Locate every blood parasite and identify its species.
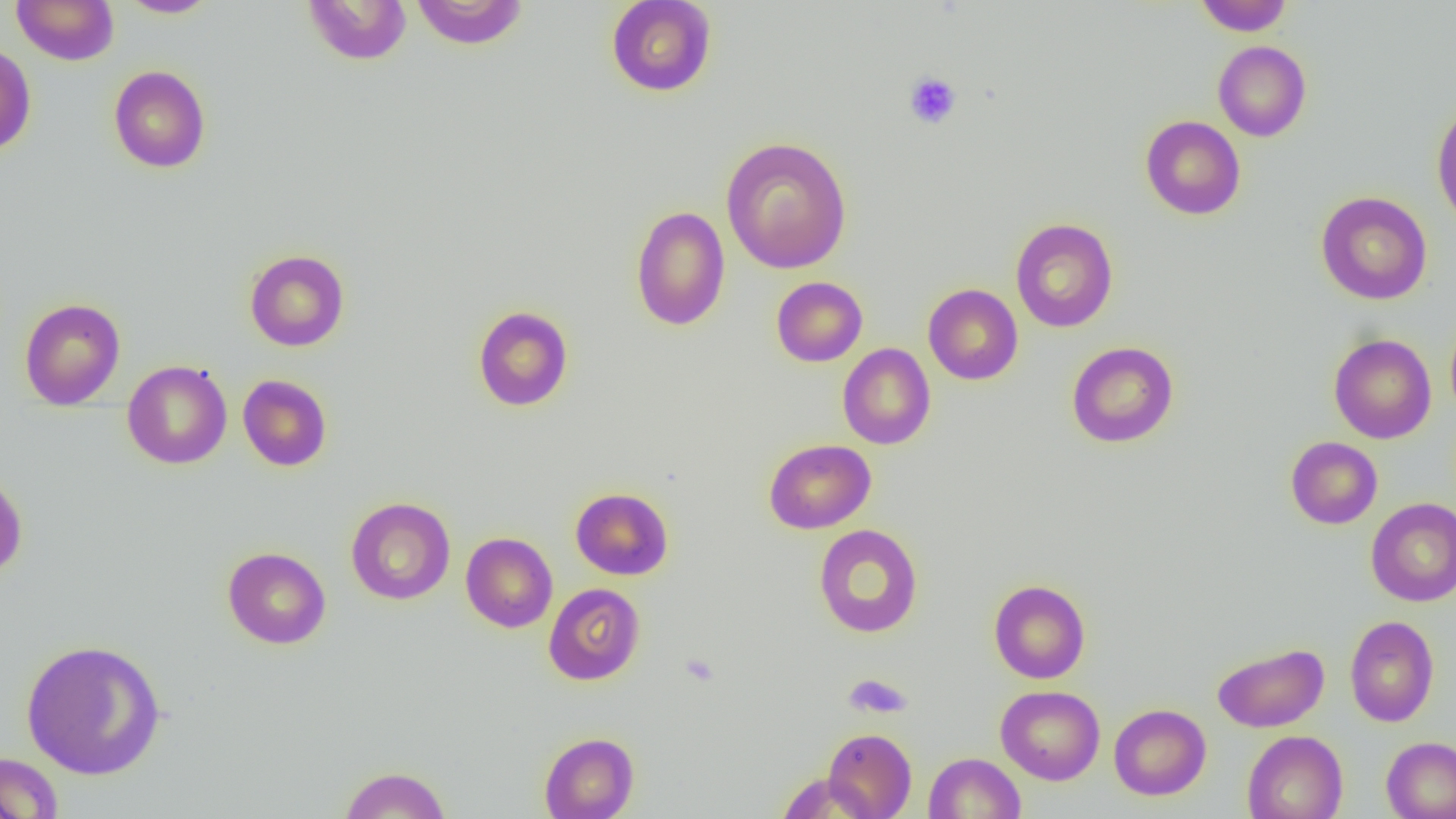

No blood parasites observed.

{
  "slide_level_diagnosis": "negative for blood parasites",
  "field_of_view": "single",
  "platelet_locations": "approximate bounding boxes as named x1/y1/x2/y2 corners in pixels: (x1=903, y1=71, x2=962, y2=129), (x1=844, y1=674, x2=912, y2=719)",
  "magnification": "1000x",
  "uninfected_red_blood_cell_locations": "approximate bounding boxes as named x1/y1/x2/y2 corners in pixels: (x1=11, y1=0, x2=119, y2=65), (x1=303, y1=0, x2=413, y2=65), (x1=410, y1=0, x2=528, y2=49), (x1=605, y1=0, x2=717, y2=97), (x1=1195, y1=0, x2=1294, y2=36), (x1=117, y1=1, x2=221, y2=18), (x1=1212, y1=40, x2=1312, y2=142), (x1=0, y1=45, x2=36, y2=157), (x1=109, y1=65, x2=211, y2=173), (x1=1431, y1=101, x2=1456, y2=231), (x1=1140, y1=115, x2=1246, y2=220), (x1=721, y1=136, x2=852, y2=274), (x1=1316, y1=191, x2=1432, y2=304), (x1=630, y1=205, x2=731, y2=331), (x1=1010, y1=217, x2=1119, y2=333), (x1=244, y1=249, x2=349, y2=352), (x1=771, y1=276, x2=868, y2=367), (x1=923, y1=284, x2=1023, y2=385), (x1=19, y1=297, x2=126, y2=411), (x1=472, y1=305, x2=574, y2=412), (x1=1445, y1=314, x2=1456, y2=420), (x1=1329, y1=334, x2=1436, y2=443), (x1=1066, y1=342, x2=1179, y2=448), (x1=837, y1=343, x2=936, y2=449), (x1=122, y1=360, x2=232, y2=469), (x1=237, y1=374, x2=332, y2=471), (x1=1285, y1=436, x2=1382, y2=529), (x1=763, y1=438, x2=876, y2=534), (x1=0, y1=468, x2=28, y2=579), (x1=570, y1=487, x2=673, y2=580), (x1=345, y1=497, x2=456, y2=605), (x1=1366, y1=498, x2=1456, y2=606), (x1=813, y1=523, x2=923, y2=638), (x1=461, y1=532, x2=558, y2=633), (x1=222, y1=546, x2=331, y2=649), (x1=988, y1=579, x2=1091, y2=684), (x1=543, y1=582, x2=645, y2=685), (x1=1345, y1=615, x2=1440, y2=727), (x1=21, y1=638, x2=167, y2=780), (x1=1212, y1=642, x2=1329, y2=732), (x1=996, y1=685, x2=1105, y2=785), (x1=1109, y1=703, x2=1211, y2=800), (x1=823, y1=728, x2=917, y2=818), (x1=1242, y1=730, x2=1348, y2=819), (x1=539, y1=732, x2=639, y2=819), (x1=1381, y1=736, x2=1456, y2=819), (x1=0, y1=752, x2=64, y2=818), (x1=924, y1=752, x2=1025, y2=818), (x1=338, y1=765, x2=451, y2=819), (x1=777, y1=772, x2=875, y2=817)",
  "image_size": "1456×819 pixels",
  "preparation": "thin blood film",
  "modality": "light microscopy"
}